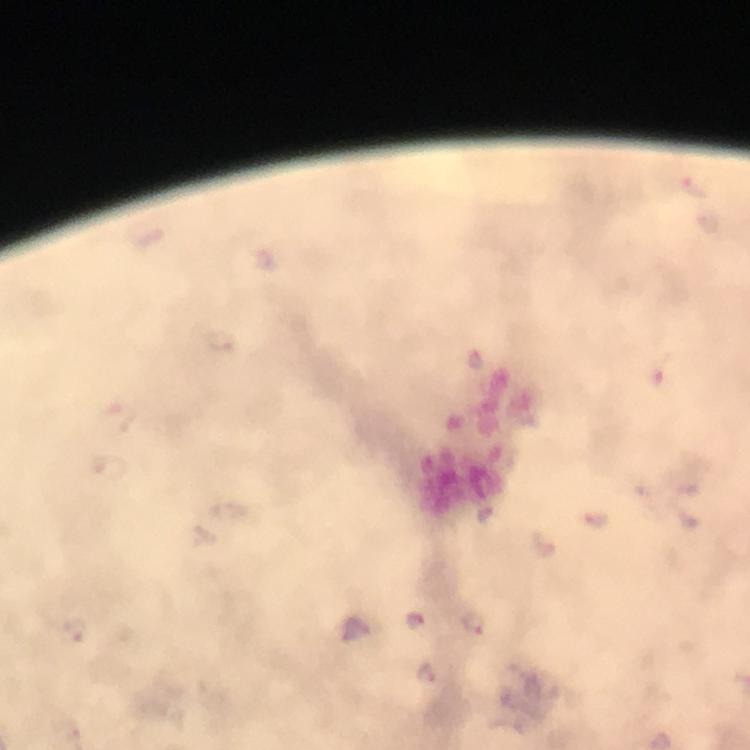

Approximate centers as (x, y) in pixels.
Summary:
  - Malaria parasite locations: (415, 619), (474, 623), (426, 673)
  - Immersion oil: applied
  - Preparation: thick smear
  - Stain: Giemsa
  - Magnification: 100x
  - Cropped from: a single field of view
  - Capture: smartphone photograph through a microscope
  - Context: from a diagnostic examination for malaria
  - Image size: 750×750 pixels